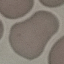
Summary:
  - Result: negative for malaria parasites
  - Preparation: thin blood smear
  - Image type: cell patch, automatically extracted from a larger field of view and resized to 64 × 64 pixels
  - Stain: Giemsa
  - Capture: smartphone camera at the microscope eyepiece